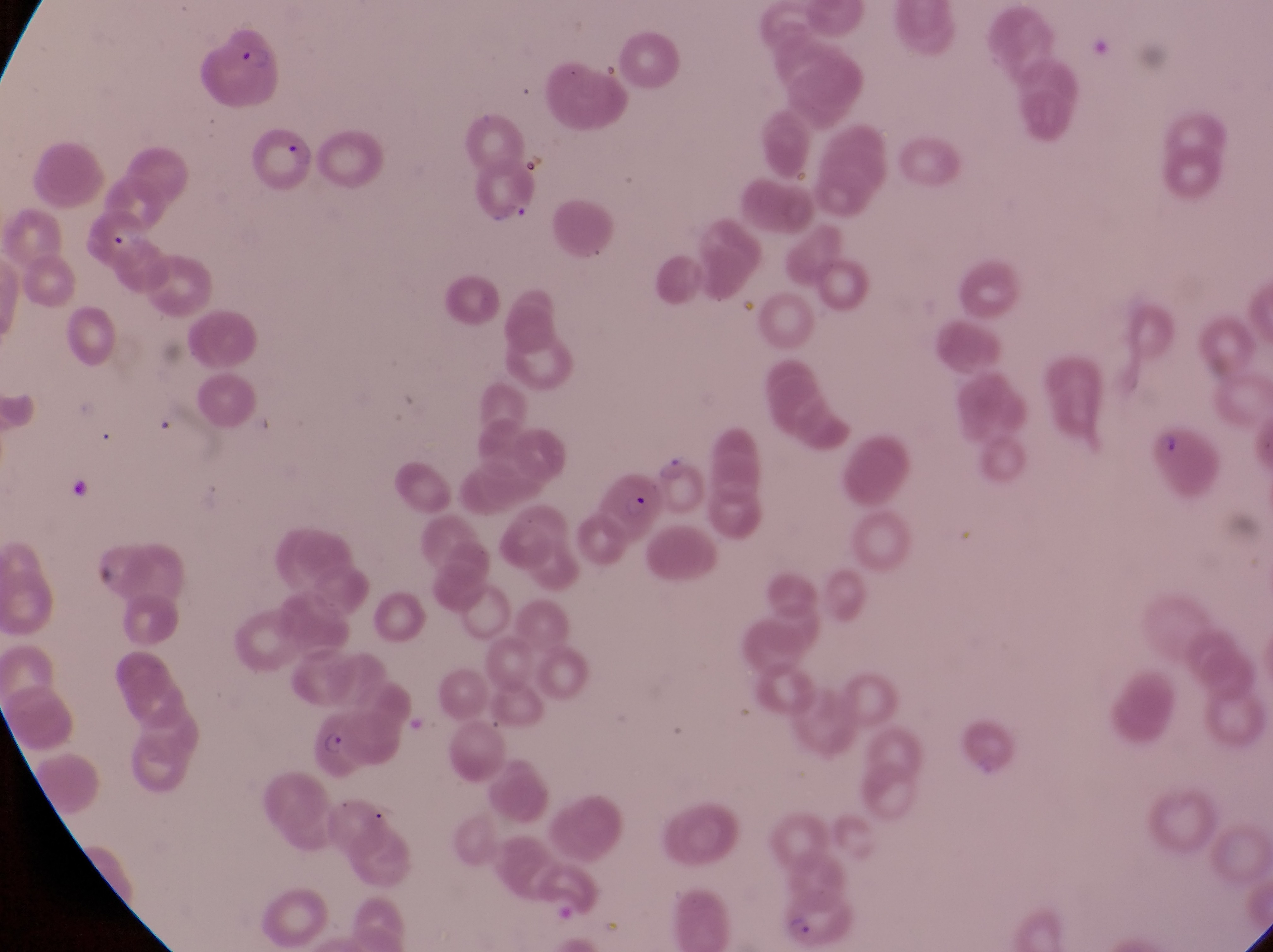

Approximate bounding boxes as (left, top, right, bottom) in pixels. Parasitised red blood cell locations: (194, 17, 281, 105), (255, 125, 313, 195), (1146, 420, 1221, 507), (597, 474, 667, 549), (314, 709, 389, 781), (779, 886, 859, 951). Captured by a smartphone held over the eyepiece of an Olympus CX-23 microscope. Thin blood film. Sample from Uganda. Single field of view. Image is 1273×952 pixels. At a magnification of 1000x.